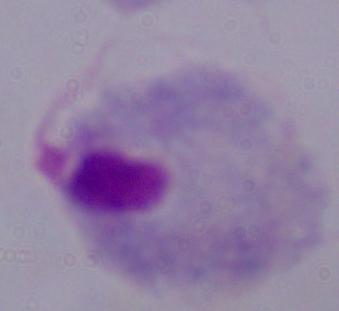

Summary:
  - Modality: photomicrograph
  - Identification: trichomonad
  - Magnification: 1000x